Assess for Plasmodium parasites.
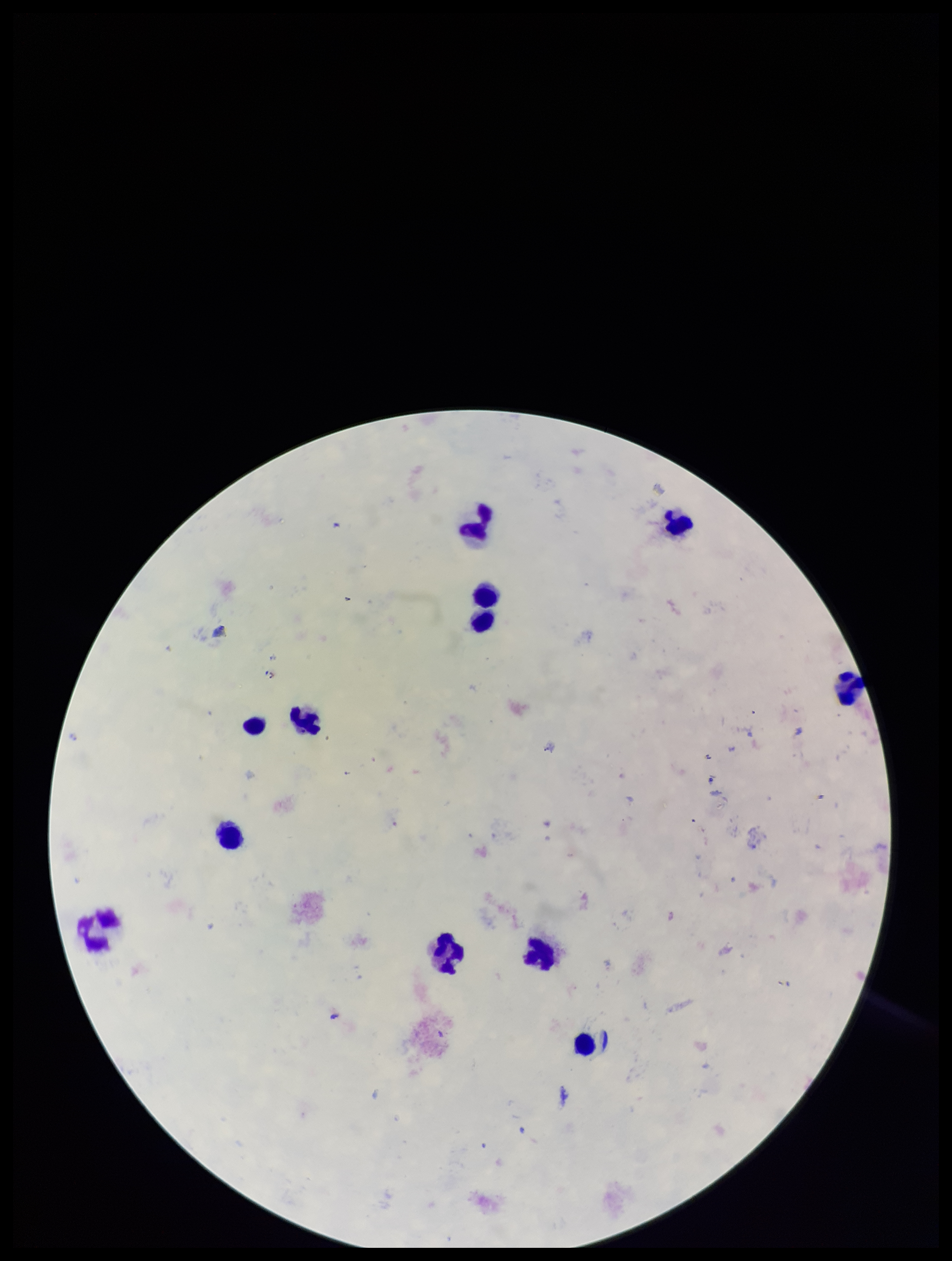
None seen.

Preparation: thick. Stained with Giemsa. One field from this slide. Photographed through the microscope eyepiece with a smartphone camera. Parasite count: 0. Image is 952×1261 pixels. Patient malaria status: negative. Leukocyte count: 12.